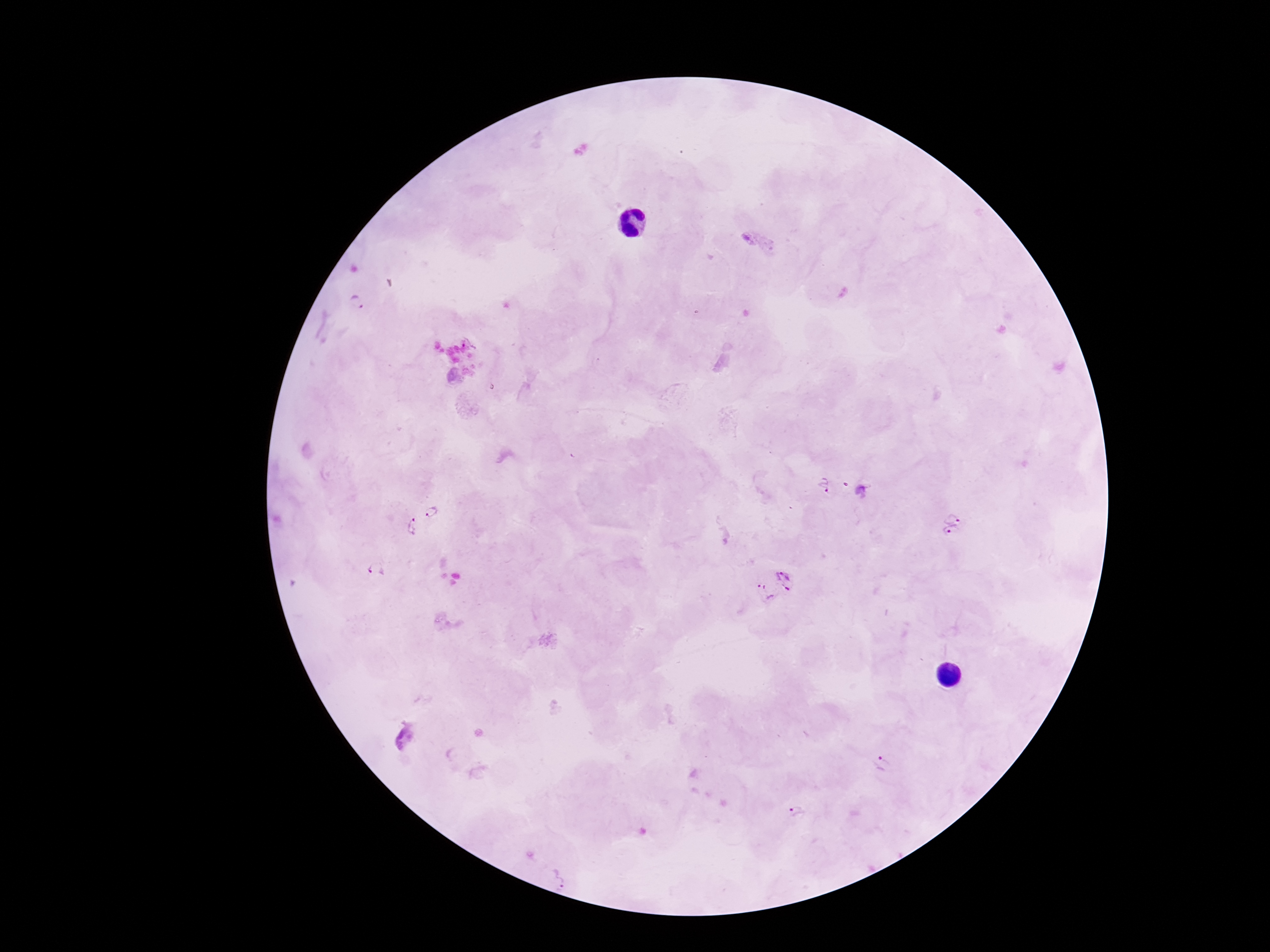

{
  "plasmodium_parasite_locations": "approximate centers as (x, y) in pixels: (357, 303), (823, 488), (862, 490), (951, 509), (435, 516), (408, 528), (948, 541), (375, 570), (787, 579), (764, 593), (403, 735), (883, 765), (798, 812), (561, 878)",
  "patient_malaria_status": "positive",
  "magnification": "100x",
  "field_of_view": "one from this slide",
  "stain": "Giemsa",
  "preparation": "thick blood film",
  "image_size": "1270×952 pixels",
  "capture": "smartphone camera through the microscope eyepiece"
}